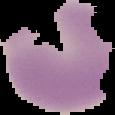
{
  "image_type": "segmented cell region on a black background",
  "malaria_status": "uninfected",
  "preparation": "thin blood smear",
  "image_size": "115×115 pixels"
}